Find the cells and give the type of each one.
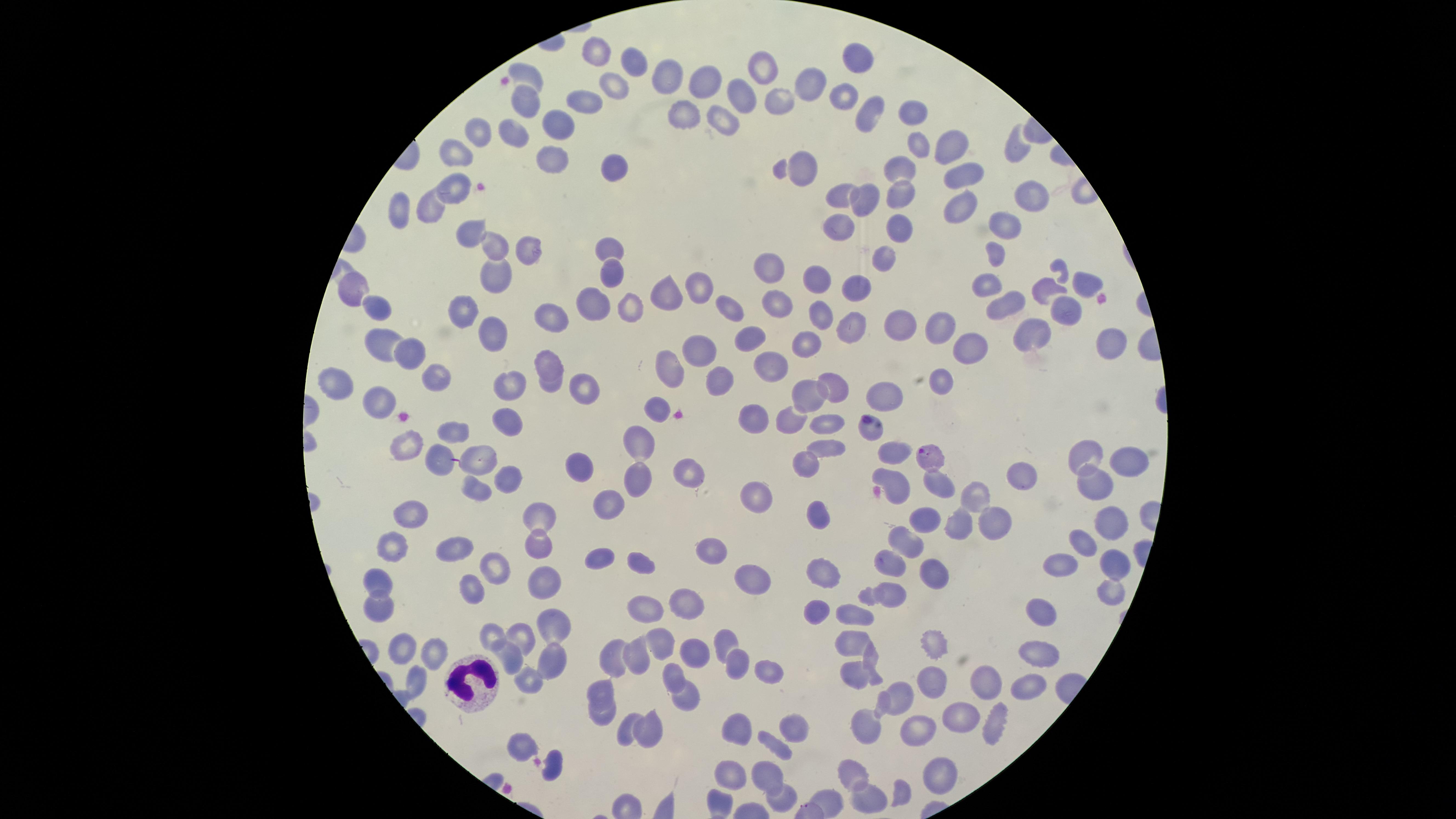
Approximate marker points as [x, y] in pixels.
Parasitized red blood cells: [926, 455].
Uninfected red blood cells: [598, 53], [858, 56], [634, 65], [766, 68], [663, 73], [531, 76], [702, 86], [807, 86], [611, 95], [526, 96], [746, 96], [841, 100], [780, 102], [580, 104], [681, 110], [912, 111], [863, 115], [720, 122], [556, 127], [516, 129], [478, 131], [919, 149], [950, 149], [1014, 150], [459, 155], [555, 161], [610, 164], [803, 168], [901, 168], [955, 180], [458, 182], [1024, 191], [832, 193], [860, 200], [902, 200], [955, 208], [433, 211], [398, 214], [1007, 222], [838, 226], [901, 230], [463, 232], [491, 248], [608, 248], [526, 252], [999, 252], [886, 266], [770, 269], [612, 275], [494, 281], [820, 282], [357, 283], [1083, 283], [697, 286], [853, 287], [986, 287], [1041, 291], [666, 297], [725, 303], [777, 303], [1005, 304], [590, 305], [377, 306], [632, 309], [1070, 310], [822, 312], [468, 313], [555, 316], [846, 327], [898, 329], [377, 331], [942, 334], [1037, 335], [493, 337], [749, 338], [807, 340], [1105, 342], [969, 349], [406, 350], [698, 350], [547, 359], [665, 365], [768, 365], [438, 373], [337, 376], [722, 380], [832, 383], [944, 383], [506, 384], [551, 385], [583, 390], [806, 394], [889, 396], [378, 400], [658, 407], [754, 418], [511, 419], [791, 420], [458, 425], [826, 425], [870, 430], [405, 439], [642, 441], [826, 451], [1079, 452], [477, 453], [897, 453], [434, 456], [1127, 457], [585, 465], [804, 466], [681, 468], [1017, 475], [509, 477], [891, 477], [640, 481], [1097, 484], [939, 485], [475, 490], [980, 490], [757, 495], [610, 510], [819, 517], [410, 518], [544, 519], [929, 522], [997, 524], [1109, 525], [962, 529], [905, 540], [1088, 540], [395, 542], [458, 547], [710, 547], [543, 550], [594, 560], [642, 562], [889, 562], [1061, 564], [1109, 564], [493, 568], [824, 573], [933, 577], [757, 583], [381, 584], [547, 586], [891, 592], [1106, 593], [469, 594], [863, 594], [383, 603], [686, 604], [646, 608], [1041, 612], [850, 613], [817, 614], [557, 620], [492, 631], [523, 636], [726, 640], [849, 640], [658, 641], [935, 644], [1035, 645], [398, 646], [433, 651], [693, 653], [510, 656], [608, 658], [642, 658], [869, 658], [737, 662], [548, 663], [763, 670], [670, 674], [852, 680], [416, 681], [532, 681], [985, 683], [1032, 685], [927, 690], [602, 692], [900, 698], [686, 700], [881, 705], [960, 716], [602, 718], [996, 723], [863, 728], [739, 731], [792, 731], [922, 731], [647, 733], [624, 736], [775, 746], [851, 766], [761, 769], [934, 769], [729, 773], [898, 793], [866, 797], [782, 799], [825, 800].
White blood cells: [473, 679].

{
  "image_size": "1456×819 pixels",
  "stain": "Giemsa",
  "capture": "smartphone photograph through the microscope eyepiece",
  "species": "Plasmodium falciparum",
  "preparation": "thin blood smear",
  "visible_region": "circular",
  "field_of_view": "single"
}